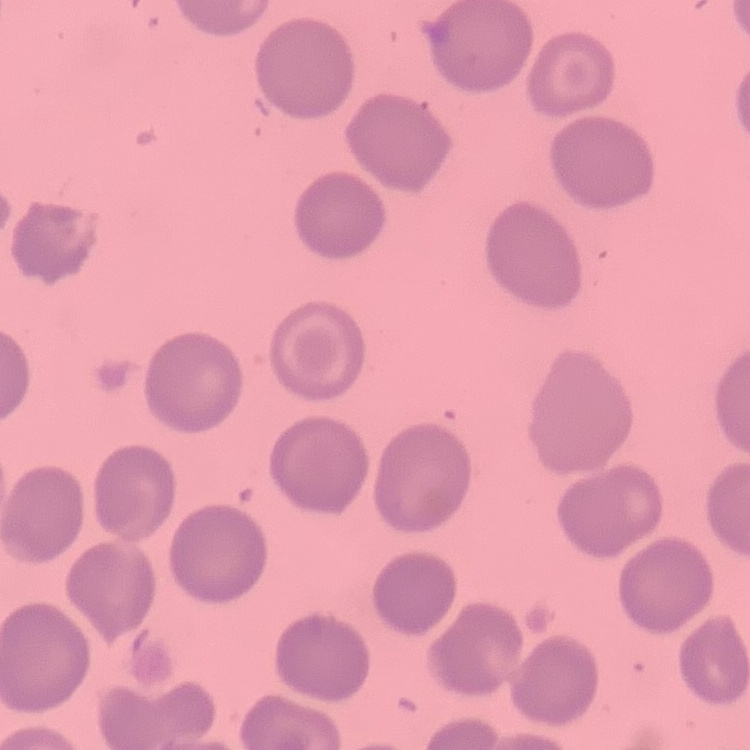
red blood cell morphology = no rouleaux formation
stain = Field's or Giemsa
image type = one tile cut from a larger photomicrograph
preparation = thin blood film